Name the cell type shown.
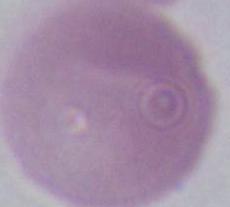

This is an erythrocyte.

Summary:
  - Modality: micrograph
  - Magnification: 1000x